Assess the morphology of the red blood cells.
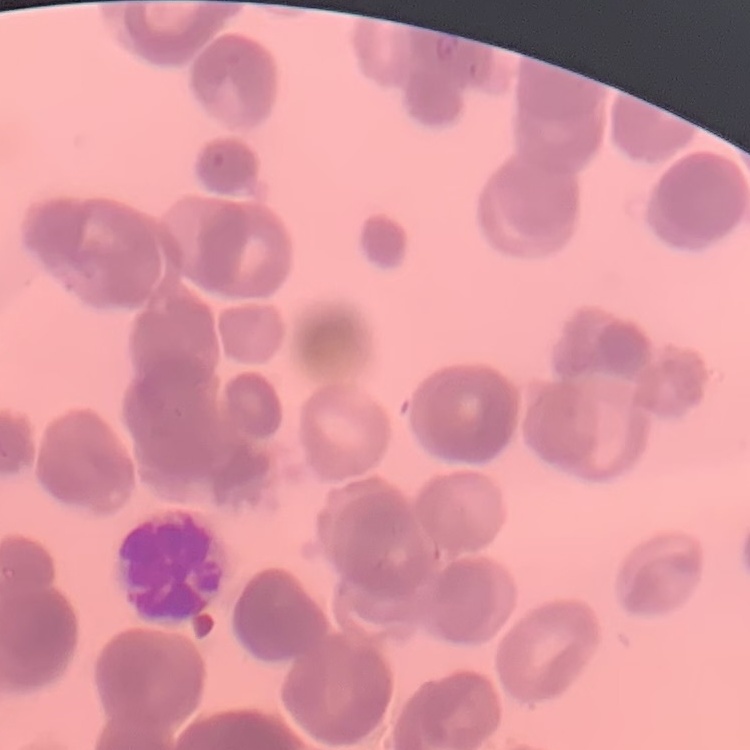
They show rouleaux formation.

Thin blood film. Square crop of a larger photomicrograph. Field's or Giemsa stain.